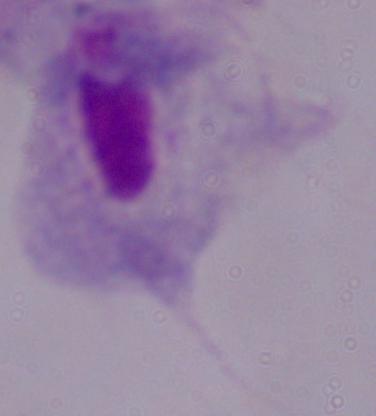
magnification: 1000x
modality: micrograph
identification: trichomonad